Name the parasite shown.
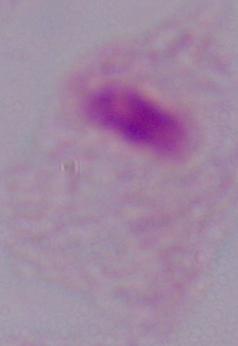
This is a trichomonad.

Summary:
  - Magnification: 1000x
  - Modality: photomicrograph